Point out each leukocyte.
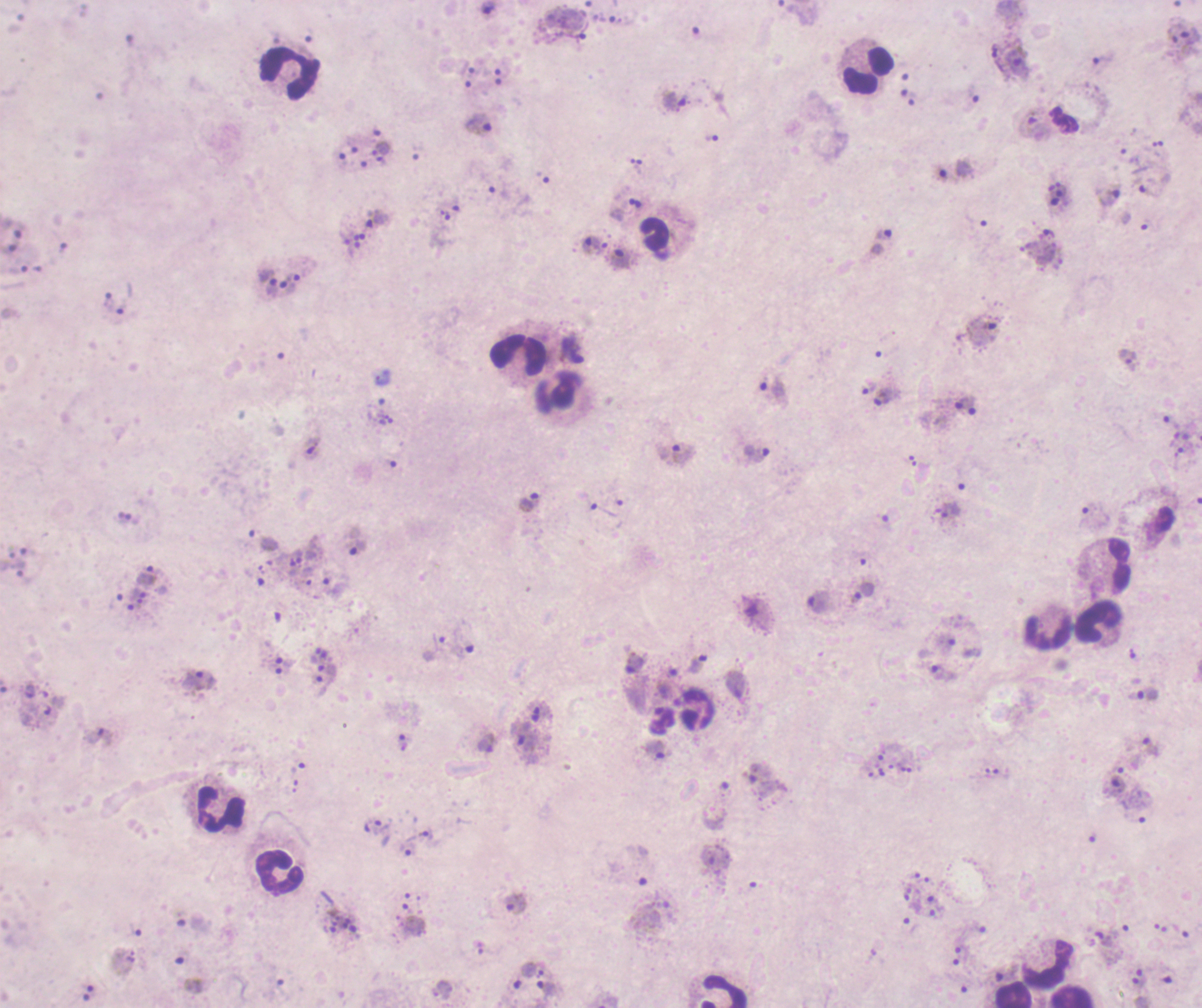

Approximate centers as [x, y] in pixels.
Leukocytes: [867, 71], [289, 76], [653, 234], [519, 354], [1118, 564], [1098, 621], [1048, 632], [219, 810], [279, 873], [1047, 963], [723, 991], [1013, 993], [1071, 996].

Approximate centers as [x, y] in pixels.
Summary:
  - Trophozoite locations: [1017, 60], [1102, 60], [676, 100], [1033, 123], [480, 127], [712, 138], [382, 148], [954, 169], [1110, 199], [635, 202], [377, 221], [882, 234], [590, 244], [620, 257], [269, 282], [983, 333], [773, 392], [887, 398], [971, 405], [313, 448], [677, 453], [757, 454], [531, 501], [946, 512], [1092, 515], [358, 547], [146, 575], [862, 593], [818, 603], [696, 662], [634, 665], [943, 673], [196, 680], [1145, 695], [535, 714], [525, 738], [403, 742], [1149, 747], [655, 751], [1114, 788], [373, 825], [514, 906], [547, 990]
  - Context: previously used in a real diagnosis
  - Stain: Romanowsky
  - Field of view: one from this slide
  - Coloration quality: bad
  - Magnification: 100x
  - Image size: 1202×1008 pixels
  - Result: positive for Plasmodium parasites
  - Background quality: poor
  - Preparation: thick smear of blood